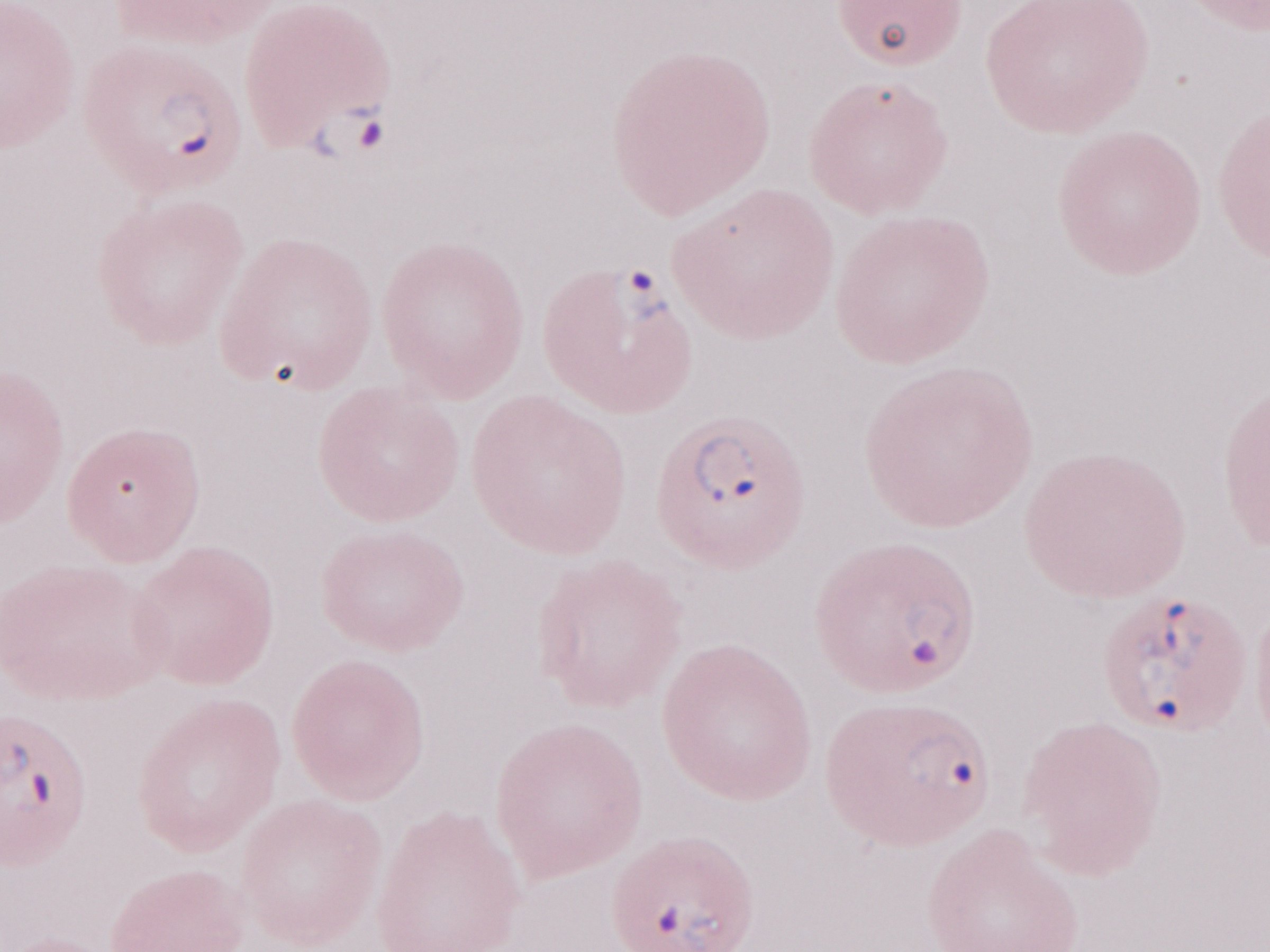
Thin blood film. Olympus BX43 microscope and DP73 digital camera. Single field of view. May-Grünwald-Giemsa stain. Image is 1270×952 pixels. Magnification: 1,000x. Malaria diagnosis (patient-level): positive.